Classify this cell by malaria status.
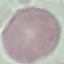

Uninfected.

image_type: cell patch, automatically extracted from a larger field of view and resized to 64 × 64 pixels
stain: Giemsa
preparation: thin blood smear
capture: smartphone through the microscope eyepiece